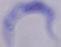

Photomicrograph. A trypanosome is shown. 1000x magnification.